Report the malaria status.
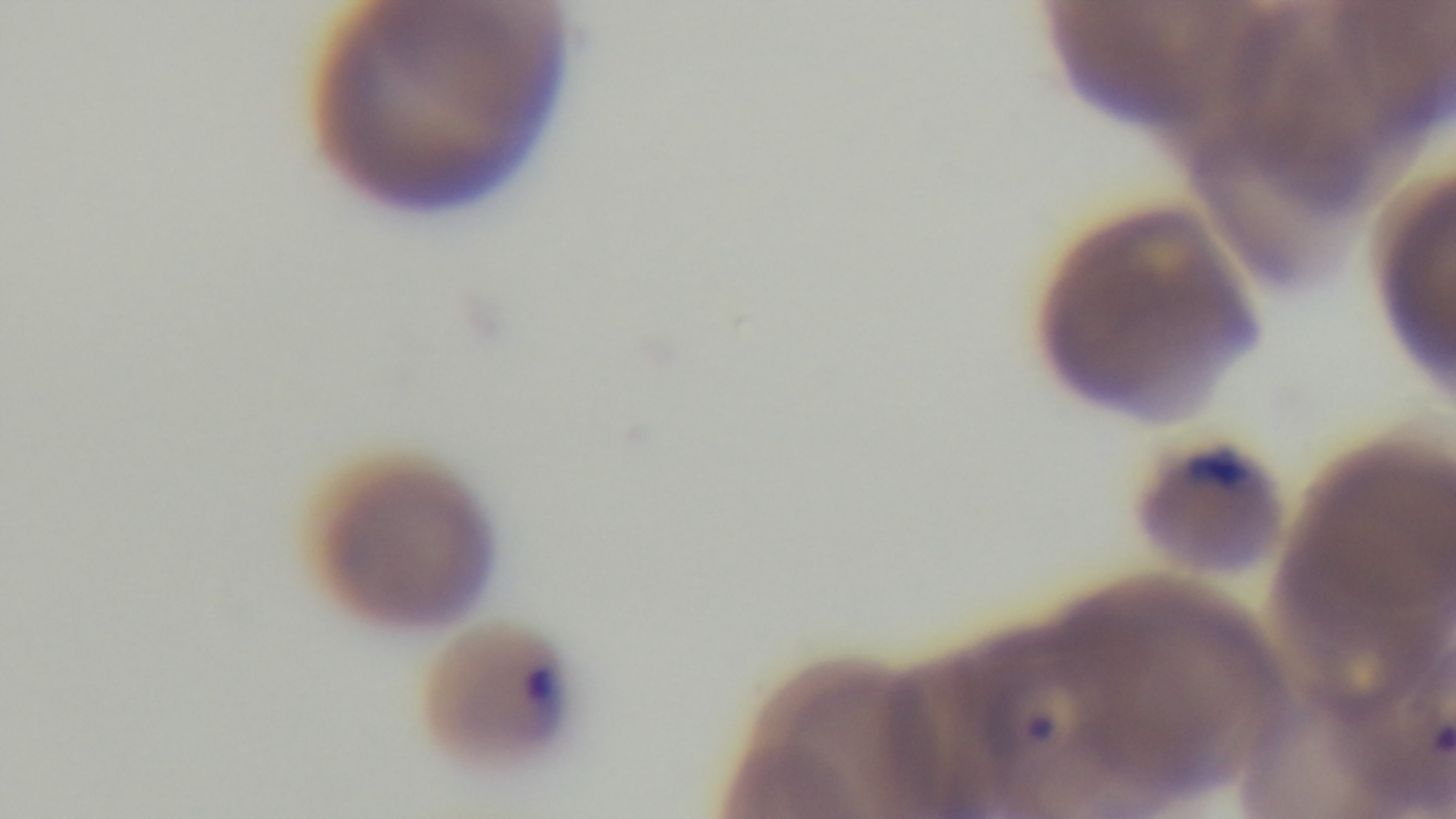
It is infected.

Captured with a mounted 4K digital camera. Single field of view. Giemsa stain. 100x oil-immersion objective. Photomicrograph. Preparation: thin.